Describe the morphology of the erythrocytes.
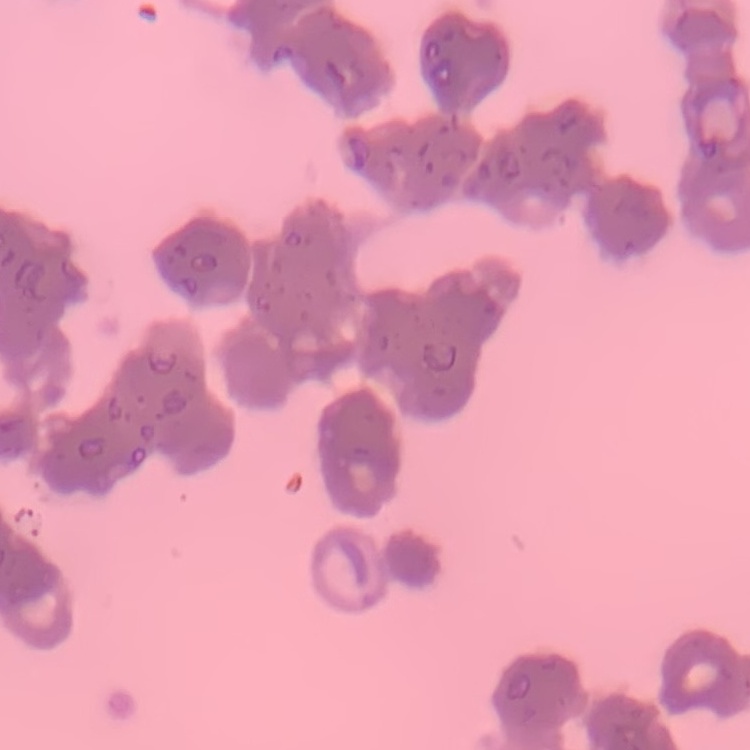

Rouleaux formation.

{
  "image_type": "square crop of a larger photomicrograph",
  "stain": "Field's or Giemsa",
  "preparation": "thin peripheral smear"
}